Describe the morphology of the red blood cells.
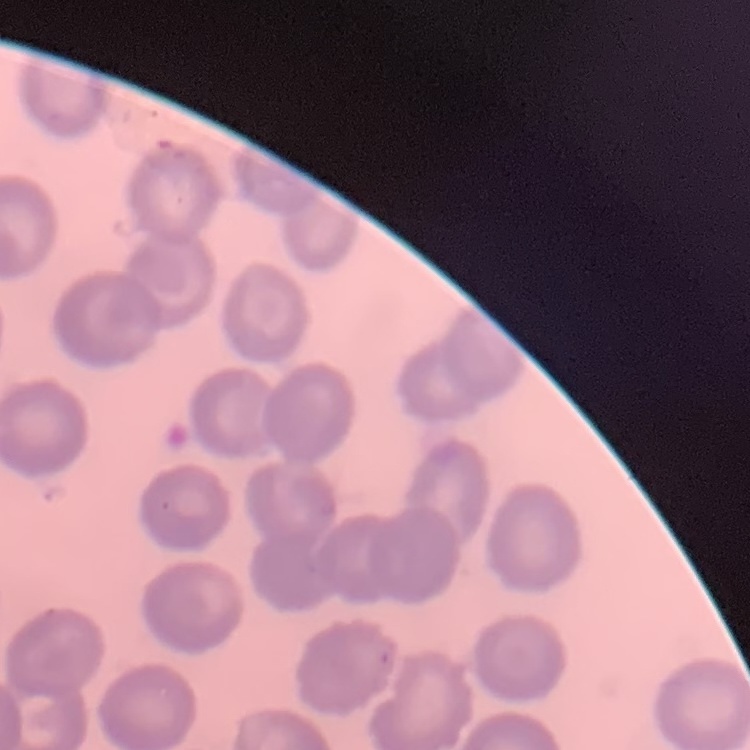
No rouleaux formation.

Summary:
  - Image type: square crop of a larger photomicrograph
  - Stain: Field's or Giemsa
  - Preparation: thin blood smear